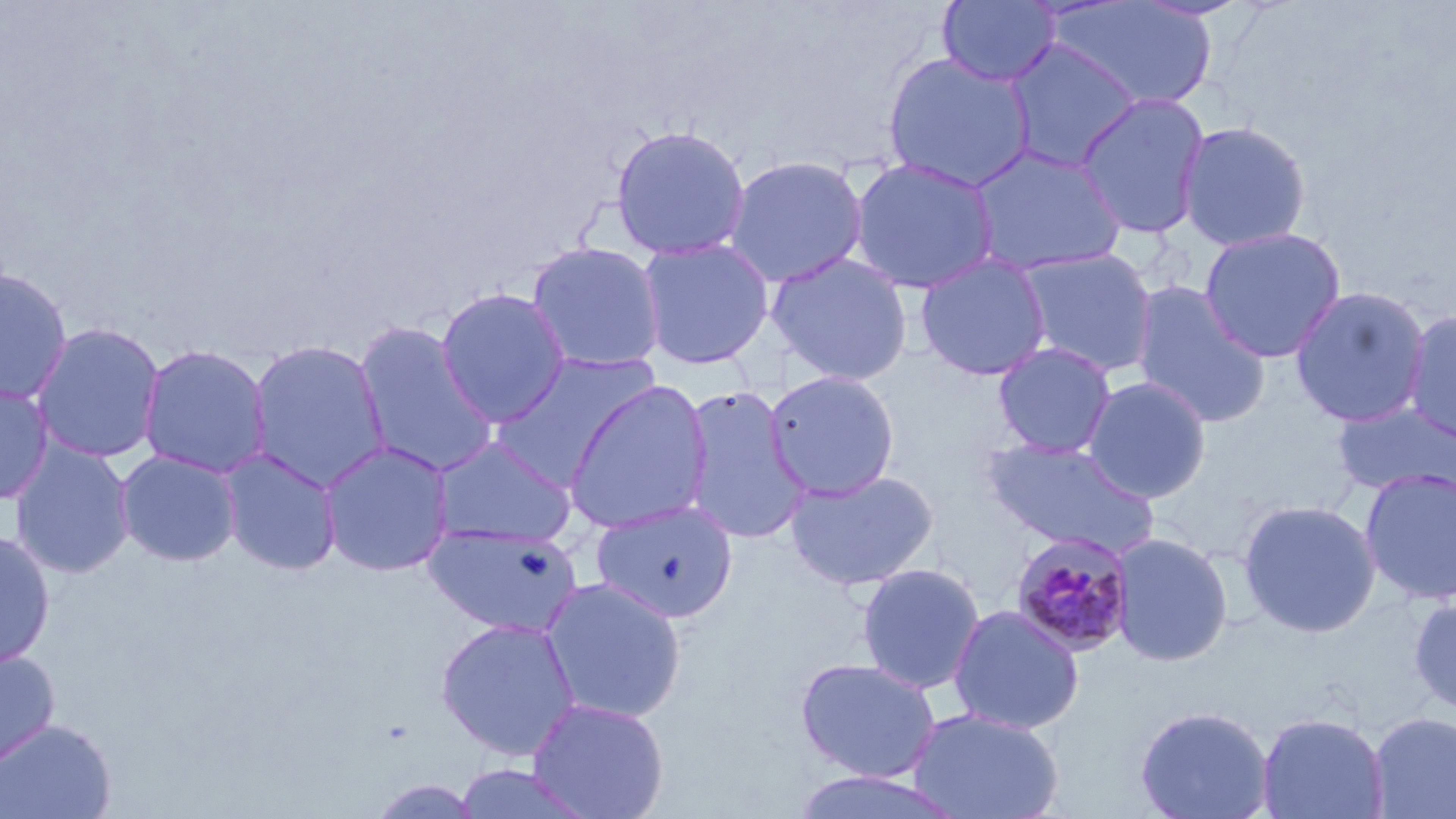
{
  "slide_level_diagnosis": "Plasmodium malariae",
  "field_of_view": "single",
  "plasmodium_malariae_infected_red_blood_cell_locations": "approximate bounding boxes as (x1,y1)-(x2,y2) corner pairs in pixels: (1010,532)-(1136,657)",
  "magnification": "1000x",
  "uninfected_red_blood_cell_locations": "approximate bounding boxes as (x1,y1)-(x2,y2) corner pairs in pixels: (937,0)-(1060,86), (1047,1)-(1219,111), (1004,38)-(1141,173), (883,52)-(1035,193), (1075,94)-(1210,240), (1177,121)-(1311,252), (610,125)-(751,261), (969,147)-(1127,277), (723,155)-(868,288), (849,157)-(999,294), (1199,227)-(1346,362), (637,238)-(774,370), (526,242)-(666,372), (1017,248)-(1159,378), (766,253)-(912,386), (915,253)-(1052,381), (0,265)-(74,405), (1132,282)-(1271,428), (1290,286)-(1431,428), (436,287)-(571,428), (1403,310)-(1456,447), (31,321)-(166,463), (353,321)-(499,478), (247,339)-(390,492), (992,342)-(1116,458), (137,343)-(272,479), (490,351)-(662,489), (764,370)-(900,501), (1082,376)-(1211,503), (0,379)-(55,505), (564,380)-(714,534), (681,388)-(811,544), (1332,402)-(1456,501), (430,436)-(577,547), (982,438)-(1160,559), (9,439)-(136,579), (319,441)-(454,577), (218,447)-(342,576), (115,449)-(243,567), (1360,469)-(1456,606), (785,470)-(938,590), (1238,499)-(1381,638), (591,501)-(738,623), (425,524)-(582,638), (0,528)-(56,670), (1110,533)-(1233,667), (856,563)-(985,694), (540,576)-(687,723), (1409,594)-(1456,715), (947,604)-(1085,734), (435,617)-(581,761), (0,646)-(60,772), (795,657)-(942,783), (527,698)-(669,819), (1134,705)-(1274,819), (907,708)-(1065,819), (1368,711)-(1456,818), (1257,712)-(1389,819), (0,718)-(117,819), (449,764)-(600,819), (790,769)-(966,818), (366,777)-(489,819)",
  "image_size": "1456×819 pixels",
  "preparation": "thin blood smear",
  "stain": "May-Grünwald-Giemsa",
  "modality": "optical microscopy"
}